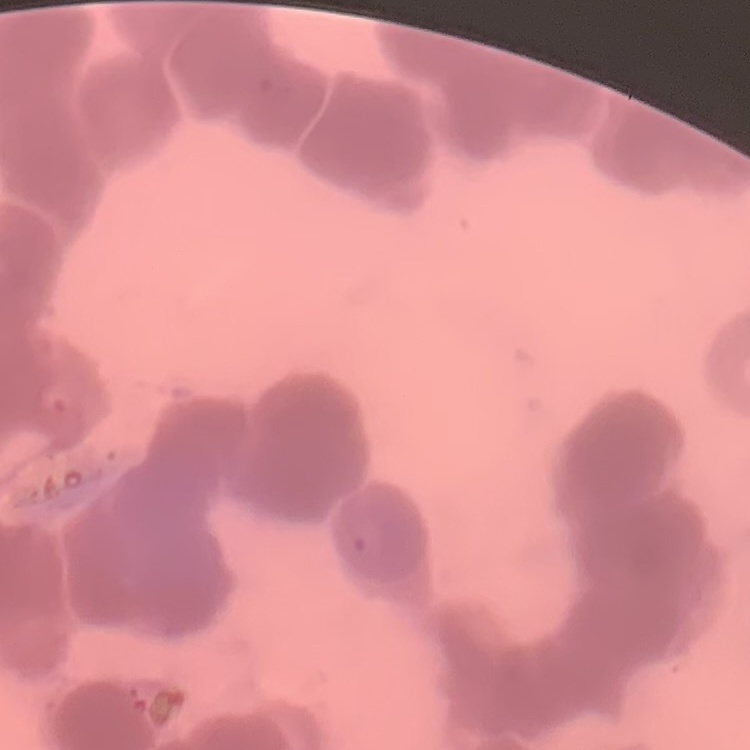
Summary:
  - Erythrocyte morphology: rouleaux formation
  - Preparation: thin peripheral smear
  - Stain: Field's or Giemsa
  - Image type: one tile cut from a larger photomicrograph